Identify the parasite.
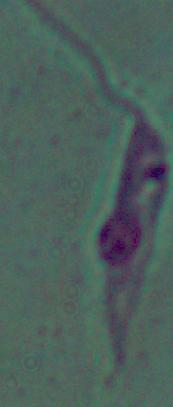

This is Leishmania.

magnification = 1000x
modality = photomicrograph